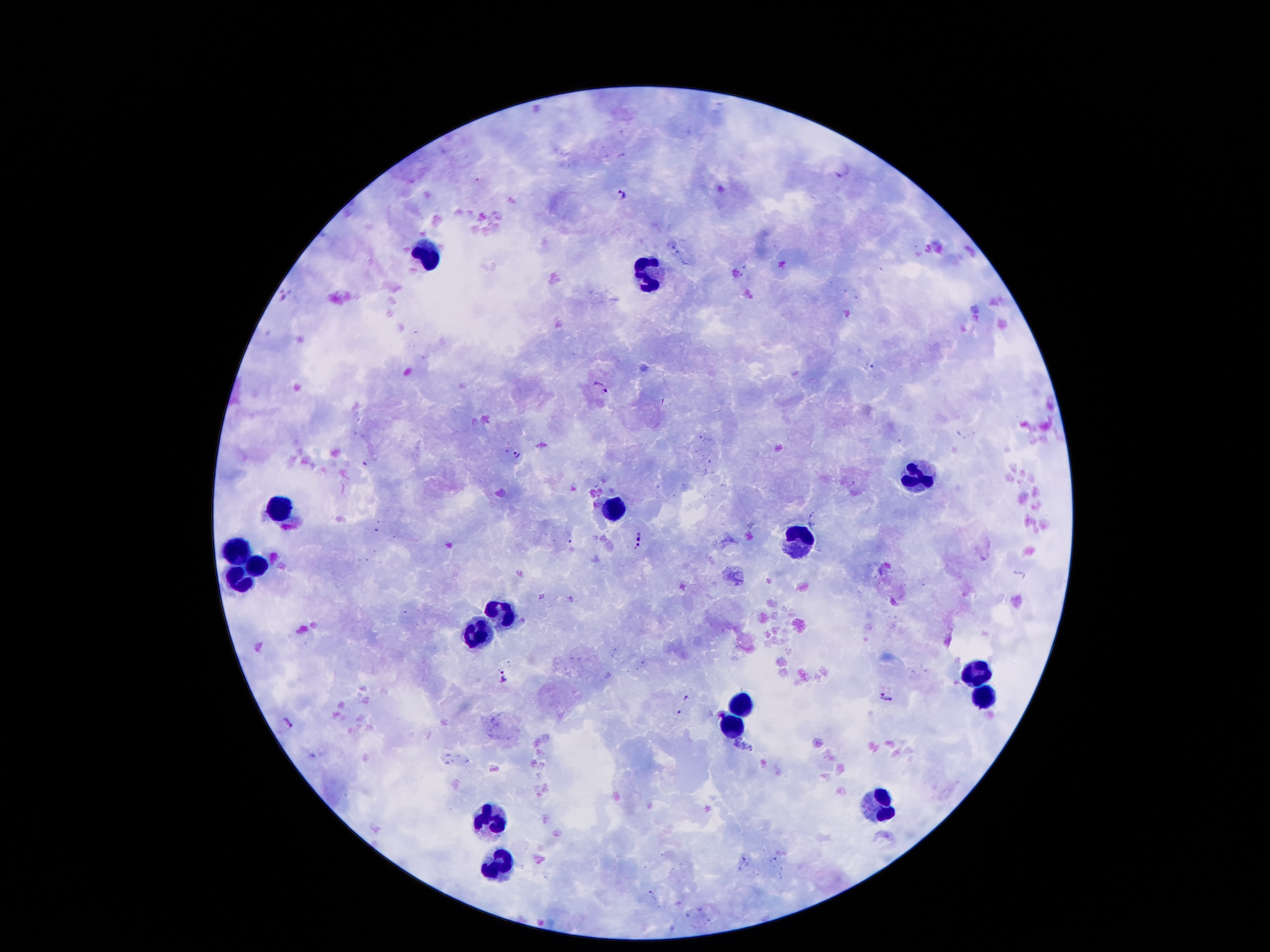
Approximate centers as [x, y] in pixels.
Summary:
  - Plasmodium parasite locations: [843, 168], [622, 194], [601, 387], [518, 456], [640, 540], [505, 676], [887, 697], [289, 722]
  - Leukocyte locations: [429, 259], [651, 279], [918, 477], [283, 508], [615, 509], [803, 540], [238, 548], [255, 567], [239, 581], [503, 610], [481, 632], [977, 674], [982, 694], [742, 705], [733, 725], [878, 806], [491, 820], [498, 864]
  - Field of view: single
  - Magnification: 100x
  - Image size: 1270×952 pixels
  - Stain: Giemsa
  - Patient malaria status: positive for Plasmodium falciparum
  - Capture: smartphone camera through the microscope eyepiece
  - Preparation: thick blood smear